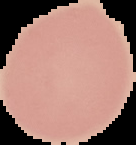 Segmented cell region on a black background. Result: no malaria parasites detected. From a thin blood film. Image is 136×145 pixels.